Give the extent of all Plasmodium ovale-infected red blood cells.
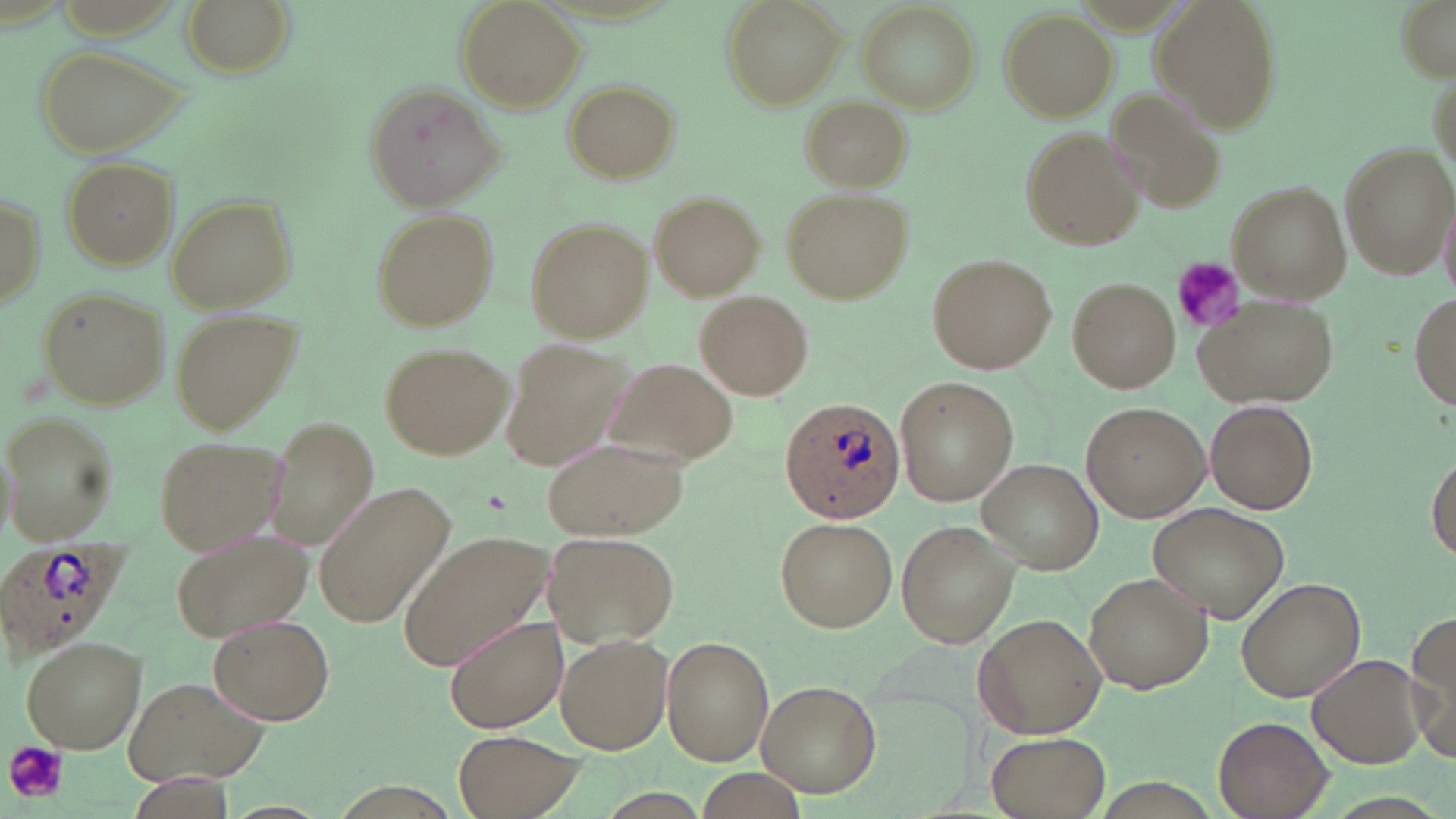
Approximate bounding boxes as (x1,y1)-(x2,y2) corner pairs in pixels.
Plasmodium ovale-infected red blood cells: (779,394)-(909,523), (7,539)-(124,654).

slide-level diagnosis = Plasmodium ovale
stain = May-Grünwald-Giemsa
image size = 1456×819 pixels
uninfected red blood cell locations = approximate bounding boxes as (x1,y1)-(x2,y2) corner pairs in pixels: (180,0)-(294,80), (454,0)-(587,114), (722,0)-(845,109), (1147,0)-(1284,129), (1394,0)-(1455,79), (858,5)-(981,110), (1001,9)-(1116,119), (34,43)-(191,158), (563,80)-(678,184), (363,82)-(510,212), (1105,86)-(1232,215), (801,97)-(911,190), (1022,128)-(1145,248), (1340,140)-(1455,279), (58,155)-(180,269), (1226,183)-(1350,302), (1,185)-(47,314), (783,189)-(914,303), (649,191)-(765,299), (1439,193)-(1456,305), (164,196)-(296,312), (373,210)-(498,331), (524,215)-(653,343), (928,254)-(1057,373), (1068,276)-(1180,393), (36,285)-(170,409), (696,289)-(813,401), (1409,289)-(1456,410), (1195,293)-(1337,408), (173,307)-(299,439), (501,339)-(631,469), (380,341)-(512,461), (605,356)-(738,467), (896,376)-(1017,505), (1206,400)-(1319,513), (1082,401)-(1209,522), (3,413)-(117,544), (264,419)-(379,549), (154,433)-(288,554), (542,435)-(690,543), (1428,454)-(1456,562), (977,461)-(1104,572), (320,484)-(451,623), (1148,501)-(1290,620), (775,516)-(896,632), (895,519)-(1018,649), (172,526)-(314,641), (399,531)-(556,670), (543,531)-(679,648), (1086,571)-(1213,693), (1237,577)-(1364,702), (972,612)-(1107,739), (1406,612)-(1456,762), (210,614)-(334,727), (444,614)-(569,733), (555,633)-(672,753), (20,635)-(147,753), (662,636)-(773,764), (1306,652)-(1428,769), (123,675)-(267,786), (756,680)-(882,797), (1212,717)-(1331,819), (453,731)-(581,819), (985,732)-(1110,818)
platelet locations = approximate bounding boxes as (x1,y1)-(x2,y2) corner pairs in pixels: (1172,256)-(1245,335), (5,741)-(68,802)
preparation = thin blood smear
magnification = 1000x
field of view = one of a larger specimen
modality = optical microscopy